Identify the parasite.
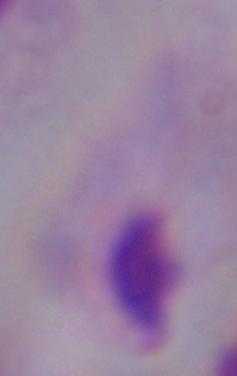

A trichomonad.

magnification = 1000x
modality = photomicrograph